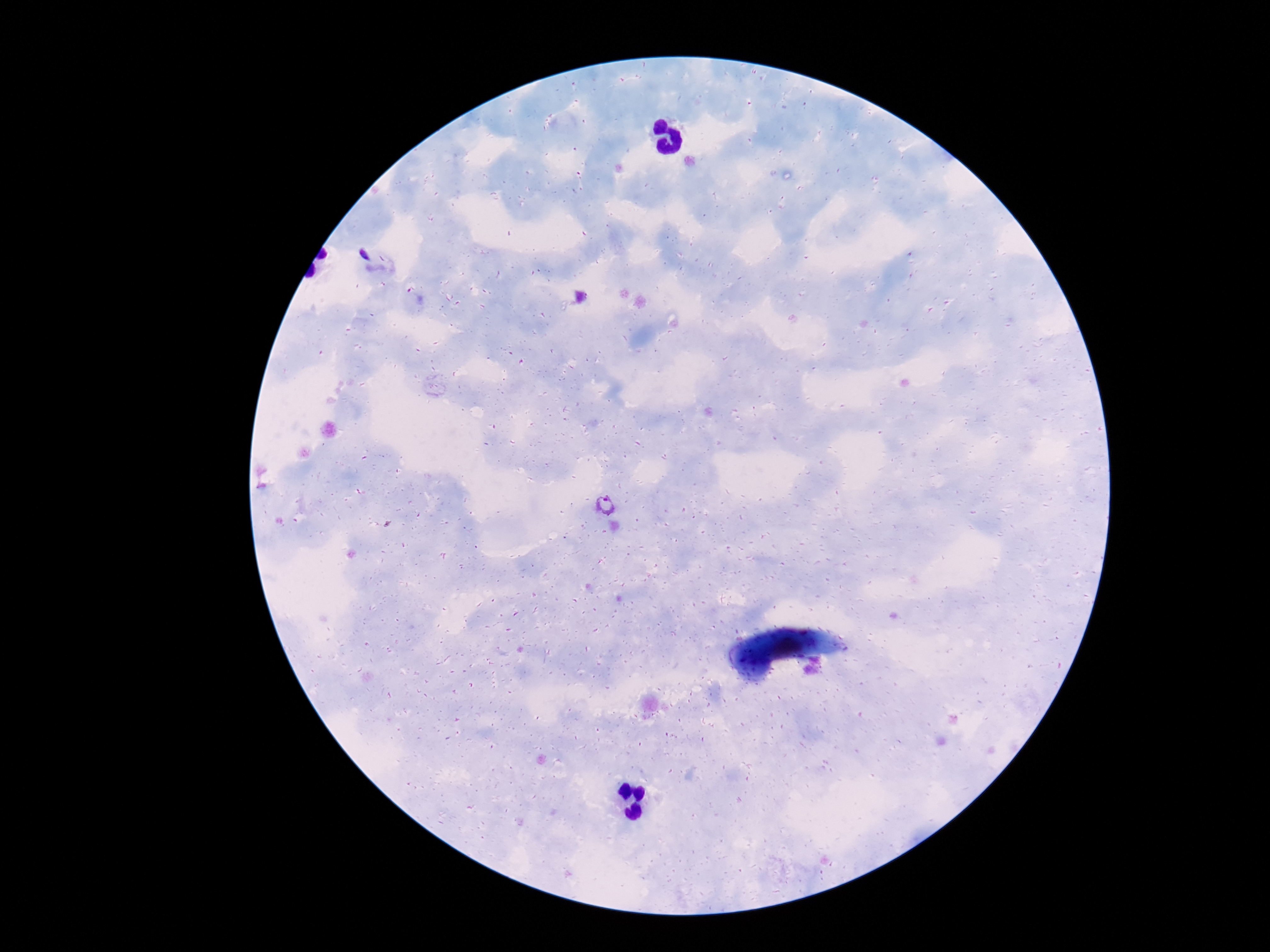

image size = 1270×952 pixels
stain = Giemsa
preparation = thick peripheral-blood smear
magnification = 100x
capture = smartphone camera through the microscope eyepiece
patient malaria status = positive
Plasmodium parasite locations = approximate centers as [x, y] in pixels: [605, 505]
field of view = one from this slide